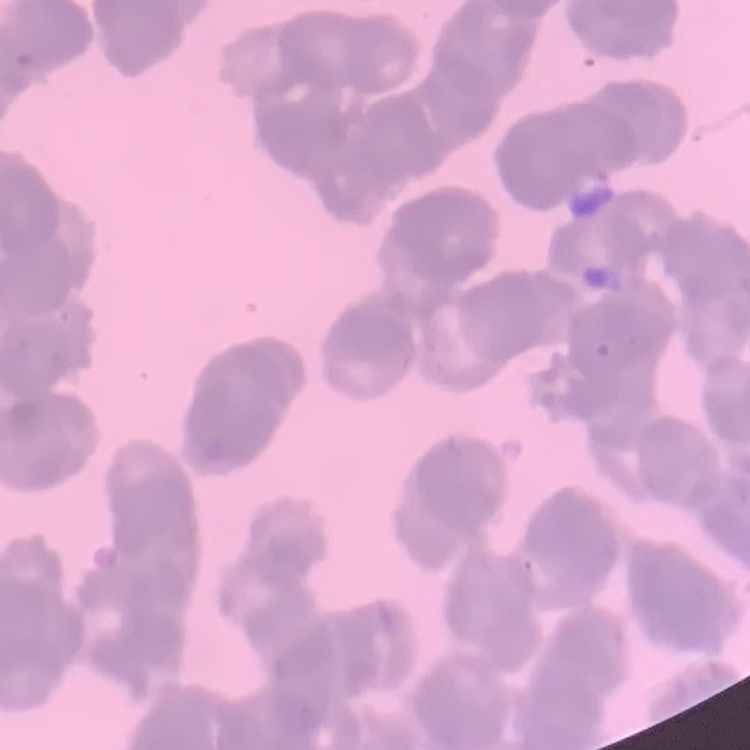 The red blood cells exhibit rouleaux formation. Field's or Giemsa stain. Square crop of a larger photomicrograph. Thin peripheral smear.